Identify the blood parasite species.
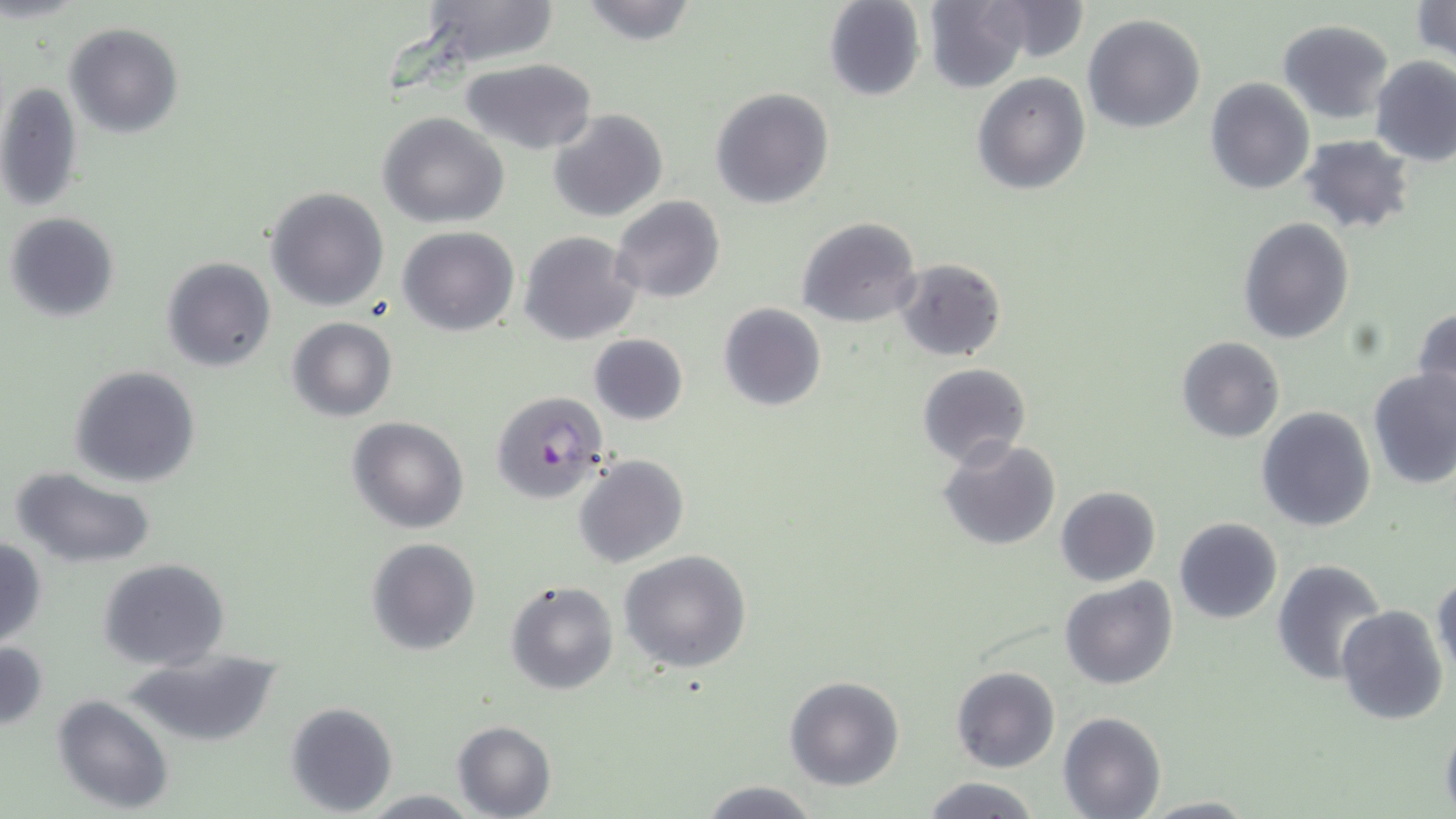

Plasmodium falciparum.

field of view = one of a larger specimen
magnification = 1000x
image size = 1456×819 pixels
stain = May-Grünwald-Giemsa
preparation = thin blood smear
uninfected red blood cell locations = approximate bounding boxes as (x1,y1)-(x2,y2) corner pairs in pixels: (408,0)-(564,72), (574,0)-(699,45), (1410,0)-(1456,63), (823,1)-(926,101), (923,1)-(1031,92), (972,2)-(1089,67), (1083,14)-(1205,133), (1278,18)-(1392,123), (63,23)-(183,137), (1370,54)-(1456,165), (462,59)-(597,155), (971,71)-(1090,194), (1205,78)-(1315,196), (1,80)-(85,213), (710,88)-(834,208), (548,108)-(668,222), (378,112)-(509,226), (1298,135)-(1416,235), (264,186)-(390,312), (610,196)-(725,304), (4,211)-(120,324), (797,217)-(921,328), (1237,218)-(1355,345), (398,227)-(519,336), (520,231)-(641,346), (159,256)-(277,371), (894,258)-(1008,361), (718,304)-(826,412), (1412,305)-(1456,417), (286,318)-(397,421), (588,334)-(689,425), (1176,336)-(1286,443), (917,363)-(1031,466), (69,365)-(201,487), (1367,369)-(1456,492), (1257,407)-(1376,532), (347,416)-(469,533), (937,437)-(1059,552), (574,454)-(689,568), (10,466)-(158,568), (1056,486)-(1161,587), (1173,517)-(1283,625), (365,537)-(481,656), (0,538)-(48,648), (618,550)-(752,675), (99,559)-(230,671), (1273,559)-(1389,685), (1432,571)-(1456,682), (1061,577)-(1179,691), (504,579)-(619,696), (1336,605)-(1450,727), (0,639)-(47,731), (124,650)-(287,749), (951,665)-(1060,773), (784,675)-(905,790), (52,694)-(175,815), (285,701)-(398,815), (1059,712)-(1167,819), (451,720)-(557,819), (1439,720)-(1456,819), (919,776)-(1042,818), (695,778)-(826,819), (361,790)-(479,818), (1136,795)-(1259,817)
Plasmodium falciparum-infected red blood cell locations = approximate bounding boxes as (x1,y1)-(x2,y2) corner pairs in pixels: (488,389)-(610,504)
modality = light microscopy